Assess this cell for malaria.
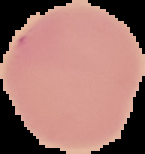
Uninfected.

image size = 145×154 pixels
preparation = thin blood smear
image type = segmented cell region on a black background